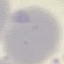 Result: negative for malaria parasites. Cell patch, automatically extracted from a larger field of view and resized to 64 × 64 pixels. Giemsa-stained preparation. Acquired by smartphone through the microscope eyepiece. Thin blood film.